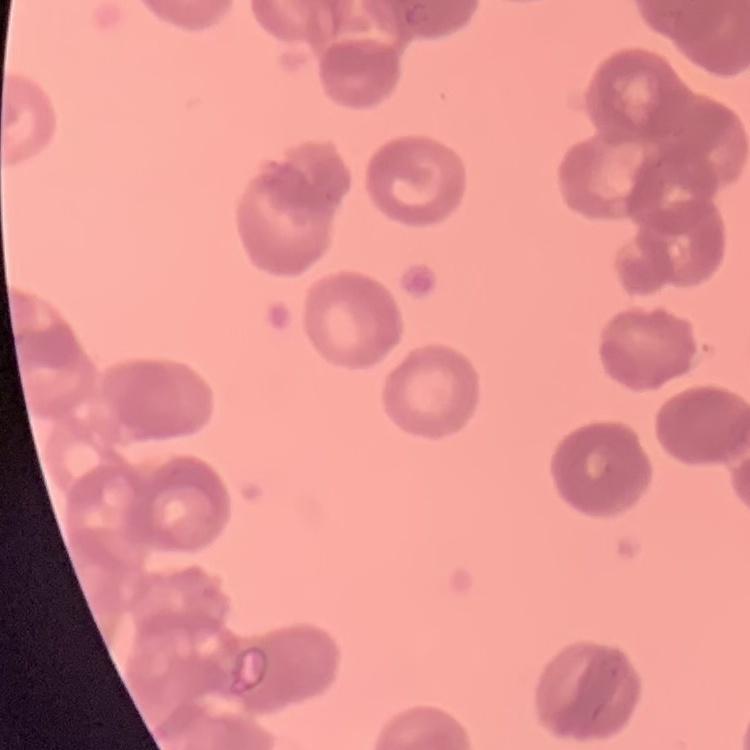
The red blood cells exhibit rouleaux formation. One tile cut from a larger photomicrograph. Field's or Giemsa stain. Thin blood smear.